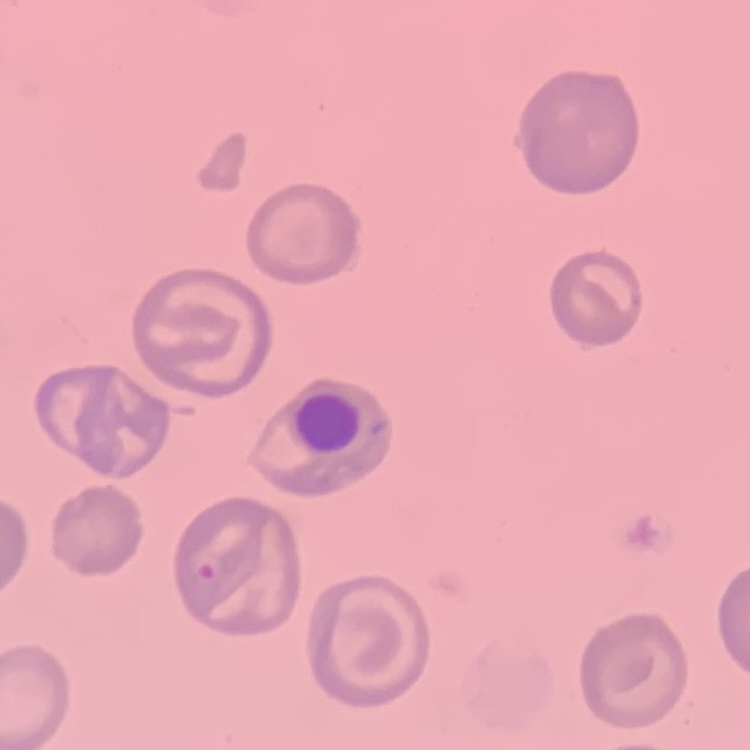

Summary:
  - Erythrocyte morphology: no rouleaux formation
  - Preparation: thin blood film
  - Stain: Field's or Giemsa
  - Image type: one tile cut from a larger photomicrograph